Give the preparation type.
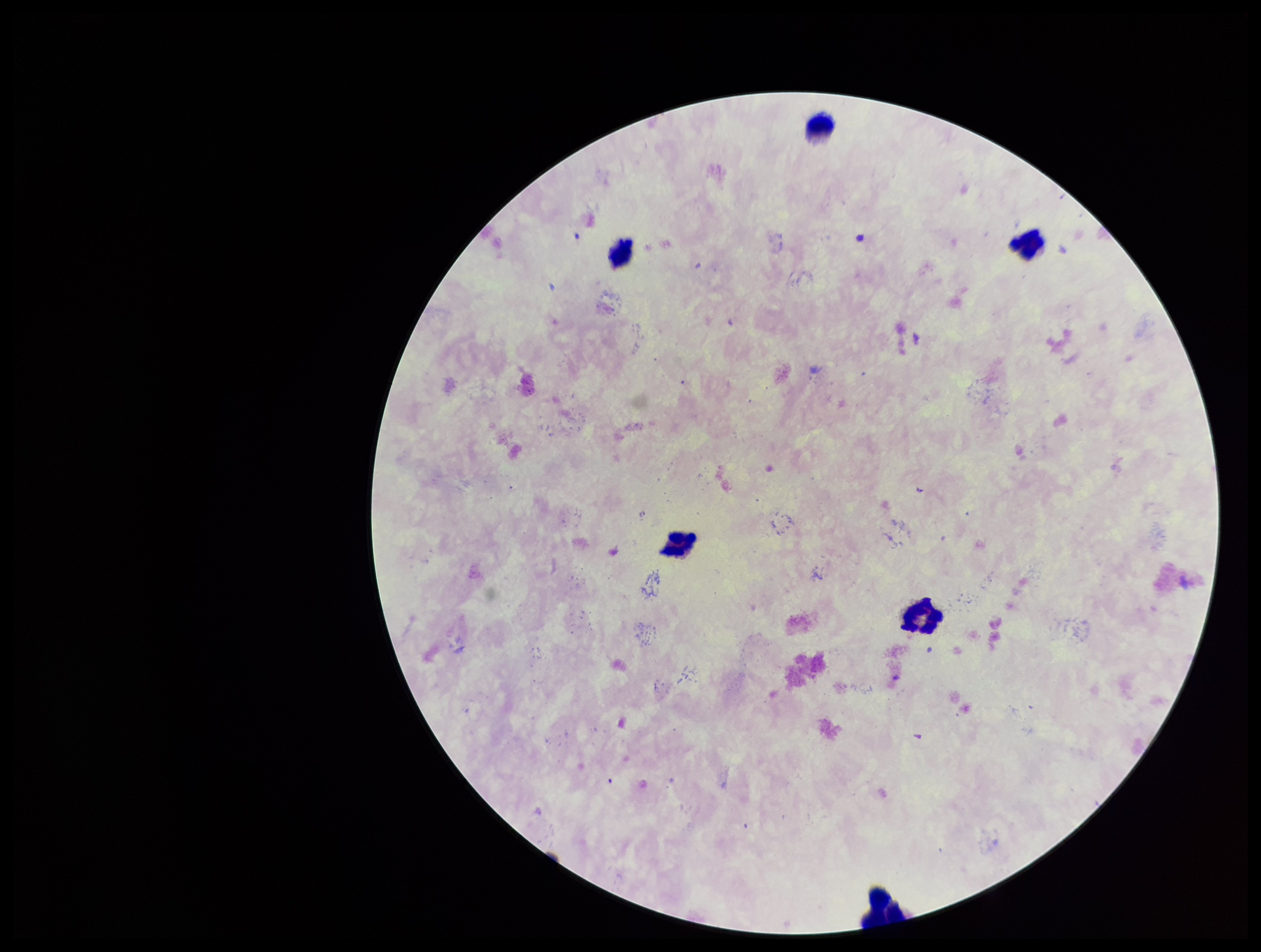
Thick.

capture = smartphone photograph through the microscope eyepiece
field of view = single
patient malaria status = negative
leukocyte count = 6
image size = 1261×952 pixels
Plasmodium parasites = none detected
stain = Giemsa
parasite count = 0